Comment on the morphology of the red blood cells.
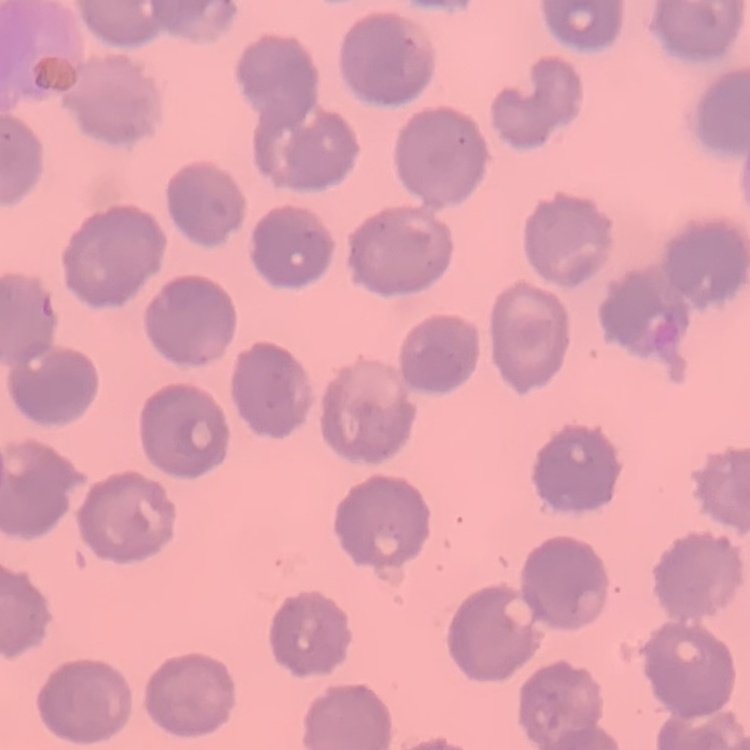

They show no rouleaux formation.

Thin peripheral smear. Stained with either Field's or Giemsa. One tile cut from a larger photomicrograph.